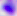 Captured at 400x magnification. Micrograph. Toxoplasma gondii is shown.